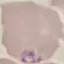
Summary:
  - Result: malaria parasites identified
  - Image type: cell patch, automatically extracted from a larger field of view and resized to 64 × 64 pixels
  - Preparation: thin blood film
  - Capture: smartphone through the microscope eyepiece
  - Stain: Giemsa